Describe the morphology of the red blood cells.
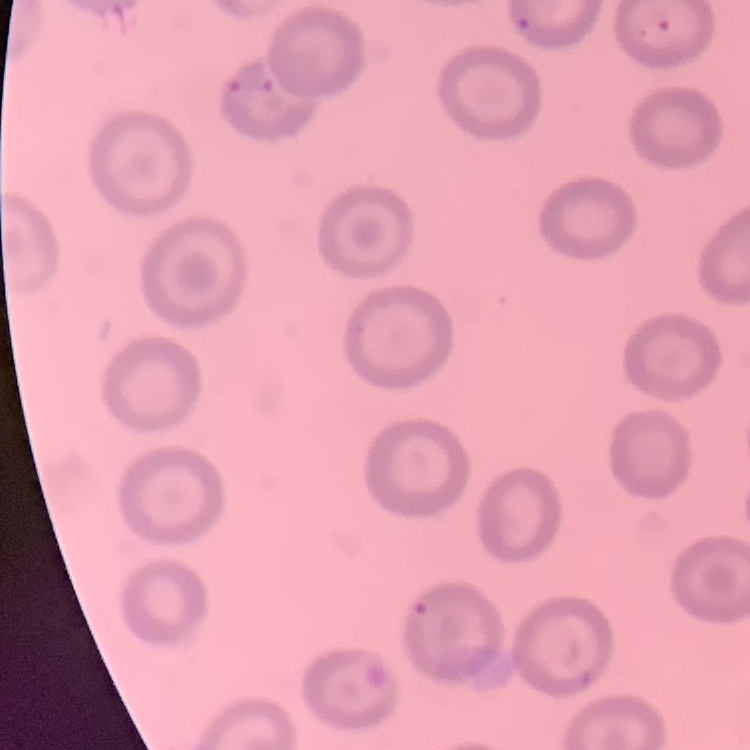
No rouleaux formation.

{
  "image_type": "one tile cut from a larger photomicrograph",
  "preparation": "thin peripheral smear",
  "stain": "Field's or Giemsa"
}